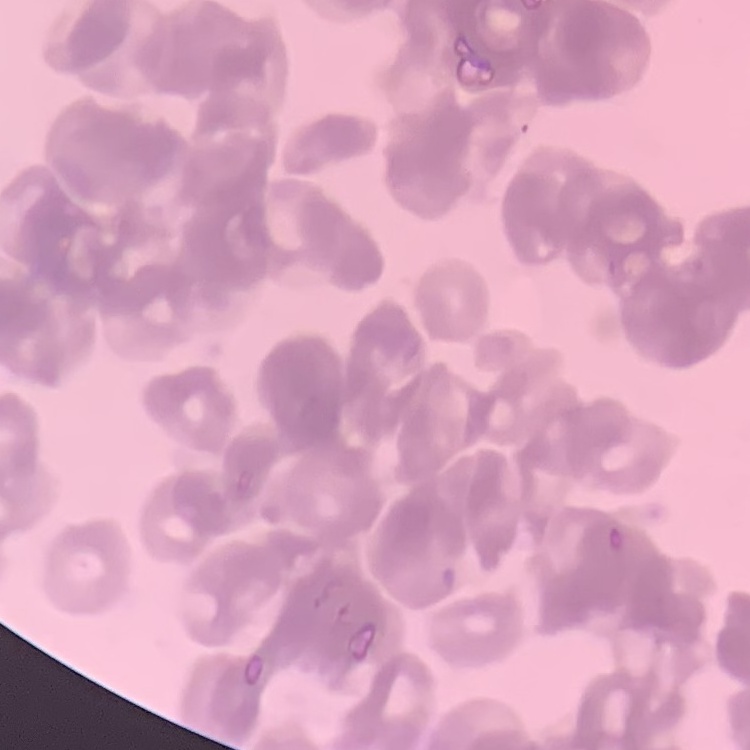
Summary:
  - Erythrocyte morphology: rouleaux formation
  - Stain: Field's or Giemsa
  - Image type: square crop of a larger photomicrograph
  - Preparation: thin peripheral smear